Comment on the morphology of the erythrocytes.
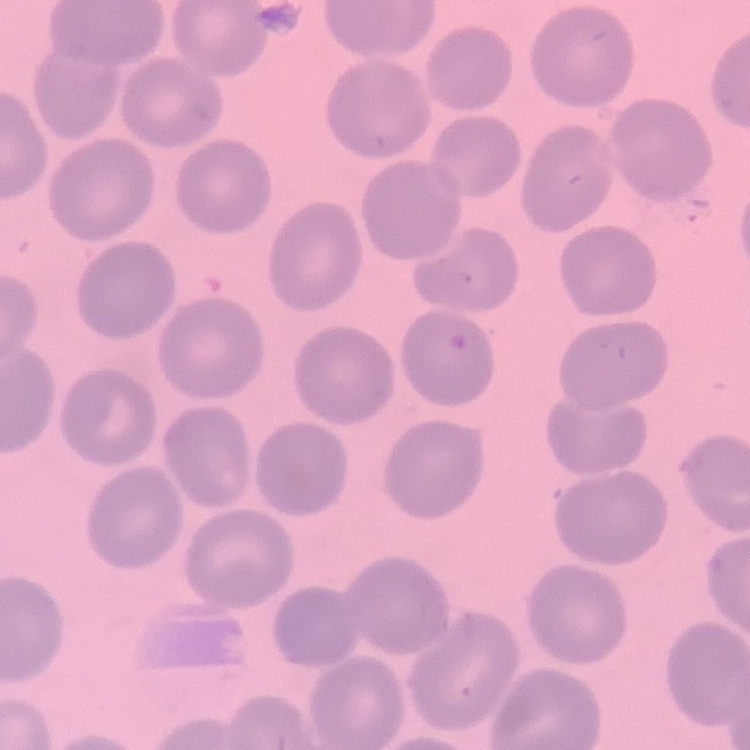
They show no rouleaux formation.

stain: Field's or Giemsa
preparation: thin blood film
image_type: square crop of a larger photomicrograph